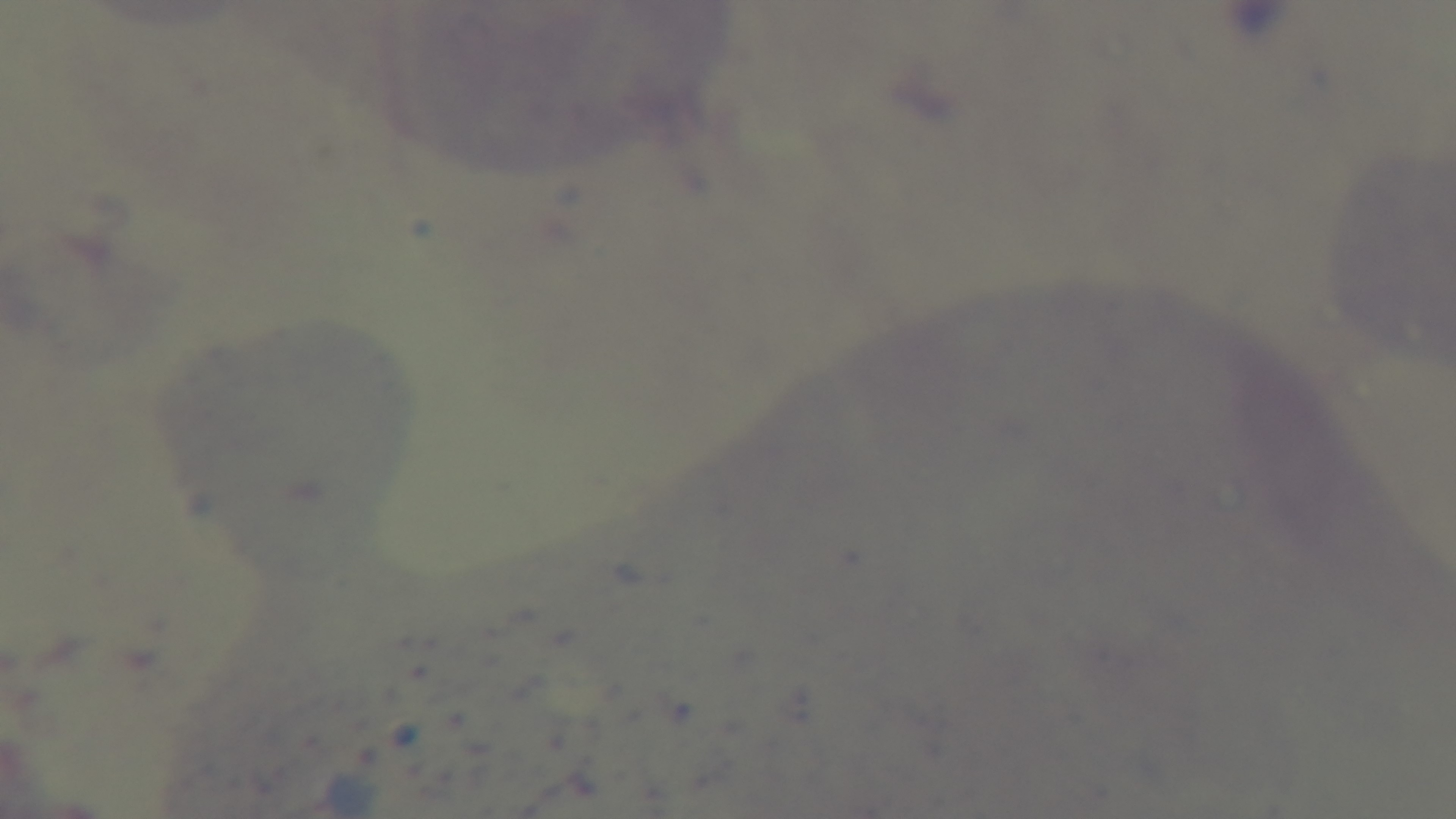
Giemsa stain. 100x oil-immersion objective. Photomicrograph. Single field of view. Preparation: thick. Malaria status: uninfected. Captured with a mounted 4K digital camera.